Report the malaria status of this cell.
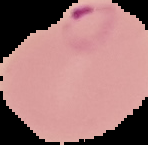

Parasitized.

preparation: thin blood smear
image_size: 148×145 pixels
image_type: segmented cell region with the area outside set to black